Comment on the morphology of the red blood cells.
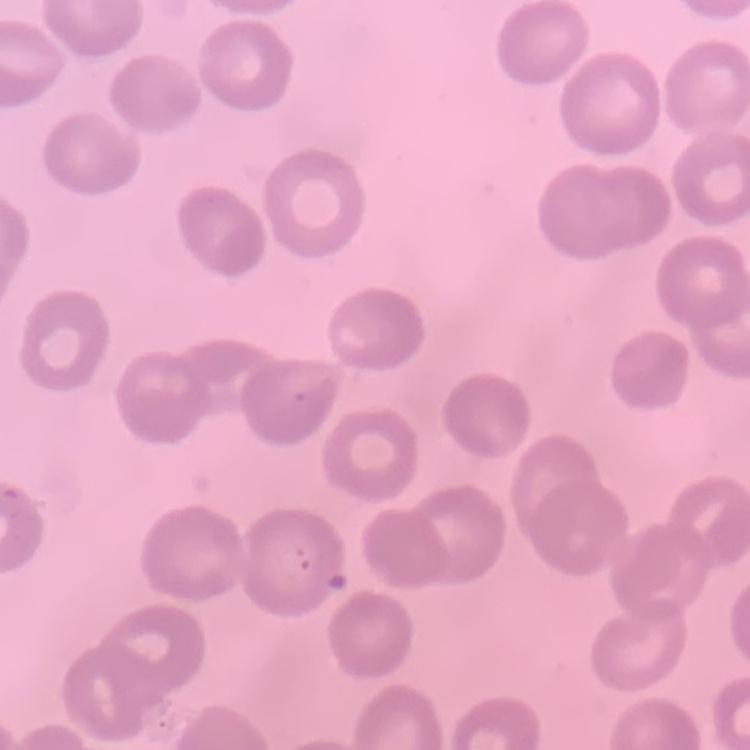

They show no rouleaux formation.

Summary:
  - Stain: Field's or Giemsa
  - Image type: one tile cut from a larger photomicrograph
  - Preparation: thin blood film